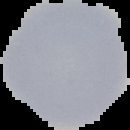
Result: no Plasmodium parasites detected. Image is 130×130 pixels. From a thin blood smear. Cell region segmented out of the field of view; the surrounding area is masked to black.